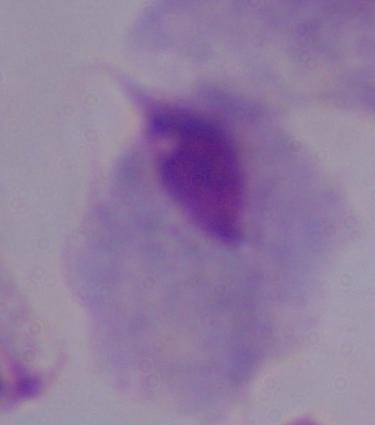

{
  "magnification": "1000x",
  "identification": "trichomonad",
  "modality": "micrograph"
}